Classify this cell by malaria status.
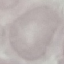

Uninfected.

Thin smear of blood. Photographed with a smartphone camera at the microscope eyepiece. Giemsa stain. Cell patch, automatically extracted from a larger field of view and resized to 64 × 64 pixels.